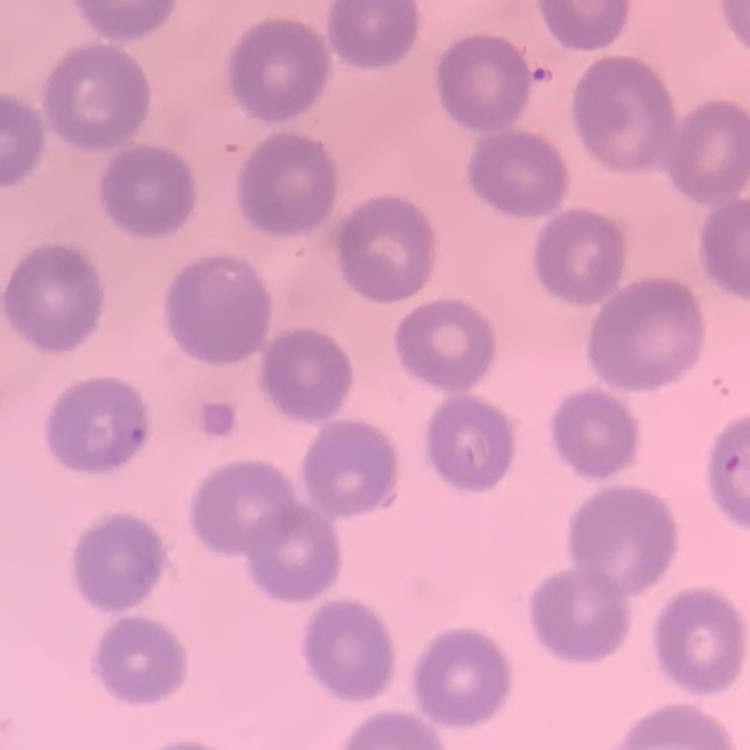
erythrocyte morphology = no rouleaux formation
image type = one tile cut from a larger photomicrograph
preparation = thin blood film
stain = Field's or Giemsa